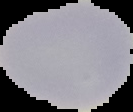

Summary:
  - Malaria status: uninfected
  - Image size: 133×112 pixels
  - Preparation: thin blood film
  - Image type: cell region segmented out of the field of view; surrounding area masked to black